Identify the cell.
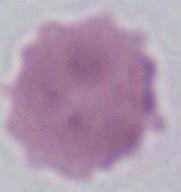
This is an erythrocyte.

Micrograph. 1000x magnification.